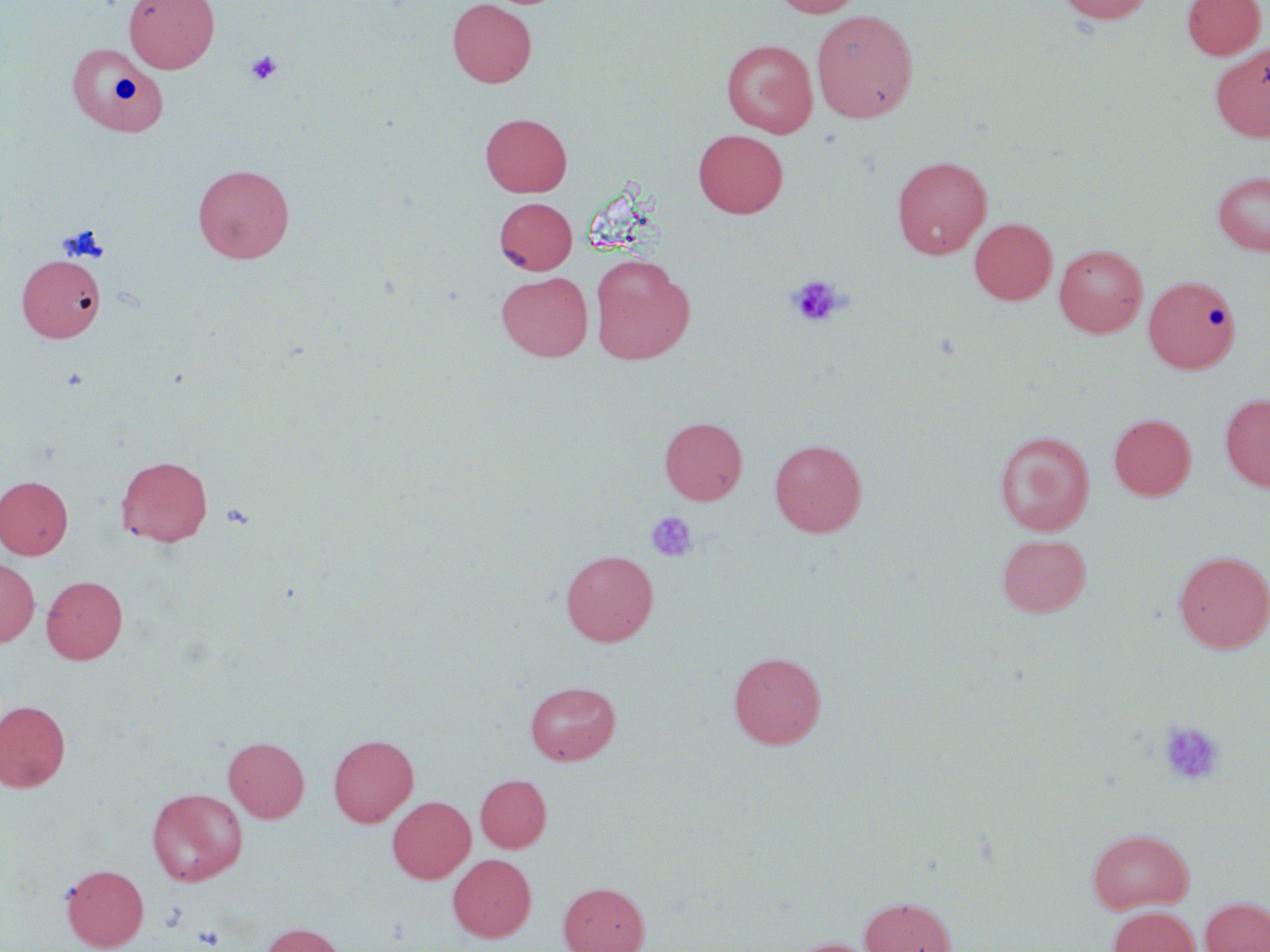
Approximate bounding boxes as named x1/y1/x2/y2 corners in pixels. Uninfected red blood cell locations: (x1=124, y1=0, x2=219, y2=73), (x1=447, y1=0, x2=536, y2=87), (x1=771, y1=0, x2=864, y2=17), (x1=1056, y1=0, x2=1153, y2=24), (x1=1182, y1=0, x2=1265, y2=59), (x1=811, y1=9, x2=919, y2=123), (x1=721, y1=39, x2=818, y2=137), (x1=64, y1=41, x2=167, y2=135), (x1=1211, y1=44, x2=1270, y2=142), (x1=480, y1=113, x2=571, y2=197), (x1=693, y1=129, x2=788, y2=218), (x1=892, y1=155, x2=992, y2=259), (x1=193, y1=163, x2=294, y2=263), (x1=1212, y1=170, x2=1270, y2=256), (x1=494, y1=197, x2=577, y2=274), (x1=969, y1=218, x2=1057, y2=305), (x1=1054, y1=244, x2=1148, y2=337), (x1=17, y1=254, x2=105, y2=342), (x1=590, y1=254, x2=694, y2=364), (x1=496, y1=271, x2=593, y2=361), (x1=1143, y1=275, x2=1241, y2=373), (x1=1220, y1=393, x2=1270, y2=492), (x1=1109, y1=413, x2=1196, y2=500), (x1=660, y1=416, x2=747, y2=505), (x1=994, y1=430, x2=1095, y2=536), (x1=769, y1=439, x2=867, y2=537), (x1=116, y1=455, x2=212, y2=547), (x1=0, y1=475, x2=73, y2=559), (x1=997, y1=533, x2=1091, y2=617), (x1=561, y1=549, x2=658, y2=646), (x1=1174, y1=550, x2=1270, y2=654), (x1=0, y1=556, x2=40, y2=647), (x1=41, y1=575, x2=127, y2=664), (x1=729, y1=651, x2=826, y2=749), (x1=524, y1=680, x2=621, y2=765), (x1=0, y1=700, x2=71, y2=792), (x1=328, y1=734, x2=418, y2=826), (x1=224, y1=736, x2=309, y2=822), (x1=476, y1=774, x2=551, y2=852), (x1=147, y1=787, x2=248, y2=886), (x1=387, y1=795, x2=475, y2=883), (x1=1087, y1=828, x2=1194, y2=914), (x1=448, y1=854, x2=536, y2=941), (x1=61, y1=864, x2=149, y2=951), (x1=559, y1=882, x2=649, y2=952), (x1=859, y1=896, x2=956, y2=952), (x1=1200, y1=897, x2=1270, y2=952), (x1=1107, y1=906, x2=1201, y2=952), (x1=261, y1=922, x2=346, y2=952), (x1=785, y1=938, x2=880, y2=952). Platelet locations: (x1=246, y1=50, x2=282, y2=85), (x1=787, y1=275, x2=847, y2=328), (x1=646, y1=511, x2=698, y2=563), (x1=1159, y1=721, x2=1225, y2=787), (x1=193, y1=925, x2=225, y2=950). Slide-level diagnosis: no evidence of blood parasites. Thin blood film. One field of a larger specimen. May-Grünwald-Giemsa stain. Optical microscopy. 1000x magnification. Image is 1270×952 pixels.